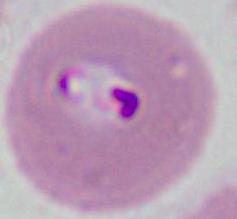
A Plasmodium parasite is seen. Captured at either 400x or 1000x magnification. Micrograph.